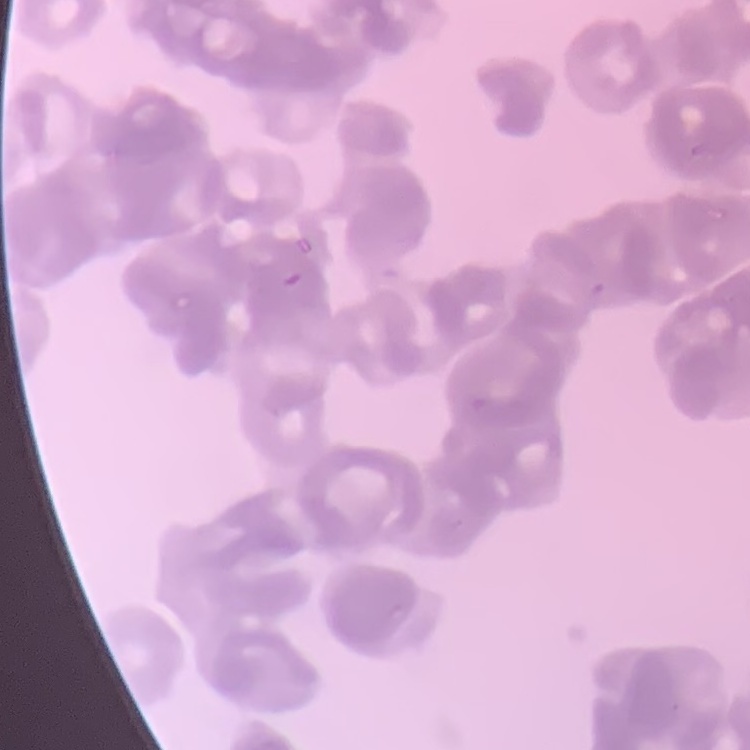

The erythrocytes exhibit rouleaux formation. Stained with either Field's or Giemsa. Square crop of a larger photomicrograph. Thin blood smear.